Classify this cell by malaria status.
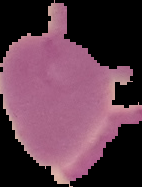
It is uninfected.

The area outside the segmented cell region is set to black. Image is 142×187 pixels. From a thin blood film.